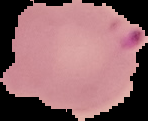
{
  "malaria_status": "parasitized",
  "image_size": "148×121 pixels",
  "image_type": "segmented cell region with the area outside set to black",
  "preparation": "thin blood film"
}